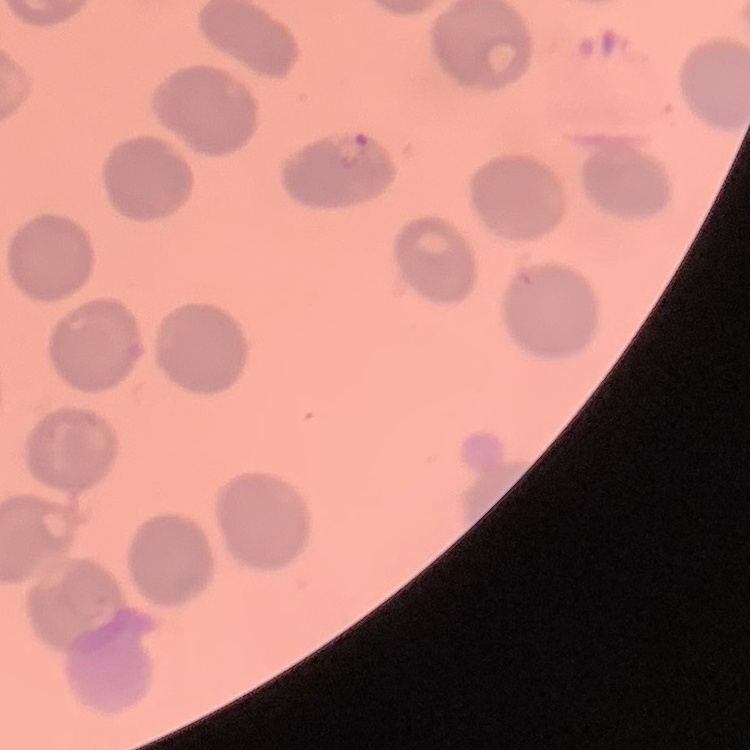
The red blood cells show no rouleaux formation. Square crop of a larger photomicrograph. Thin blood smear. Stained with either Field's or Giemsa.